Locate every uninfected red blood cell.
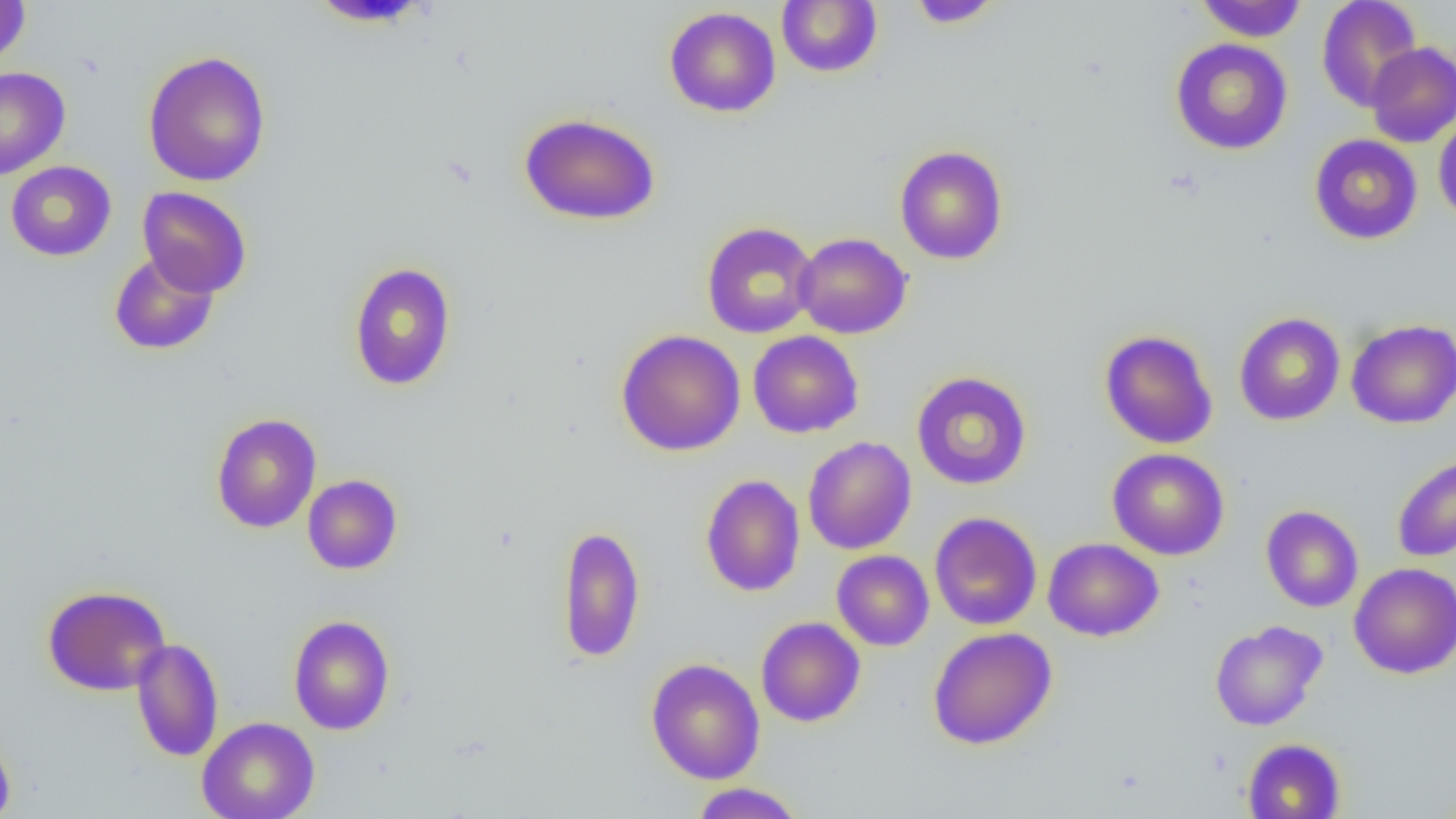

Approximate bounding boxes as (x1, y1, x2, y2) in pixels.
Uninfected red blood cells: (0, 0, 31, 68), (307, 0, 434, 27), (777, 0, 882, 77), (907, 0, 1004, 28), (1195, 0, 1307, 42), (1316, 1, 1422, 111), (664, 6, 781, 117), (1171, 38, 1293, 155), (1364, 42, 1456, 147), (142, 50, 272, 187), (0, 67, 71, 180), (519, 112, 660, 225), (1433, 113, 1456, 226), (1309, 134, 1423, 244), (894, 145, 1008, 265), (5, 161, 117, 261), (138, 186, 252, 298), (702, 222, 819, 339), (794, 232, 912, 339), (109, 251, 220, 355), (348, 261, 457, 391), (1234, 312, 1345, 426), (1347, 318, 1456, 429), (615, 329, 746, 456), (1099, 329, 1218, 449), (748, 330, 864, 438), (912, 370, 1032, 490), (211, 413, 322, 533), (802, 436, 916, 554), (1107, 448, 1230, 560), (1392, 453, 1456, 562), (700, 473, 805, 597), (303, 474, 402, 575), (1260, 505, 1363, 612), (929, 511, 1042, 631), (557, 523, 646, 663), (1043, 537, 1163, 641), (832, 550, 935, 651), (1349, 562, 1456, 679), (42, 585, 171, 696), (288, 614, 395, 735), (755, 617, 866, 727), (1210, 620, 1328, 730), (928, 626, 1058, 750), (131, 637, 224, 762), (645, 657, 765, 784), (197, 716, 320, 819), (0, 727, 16, 819), (1242, 738, 1346, 819), (689, 783, 806, 818).

Slide-level diagnosis: negative for blood parasites. Image is 1456×819 pixels. 1000x magnification. Thin blood film. Light microscopy. One field of a larger specimen.